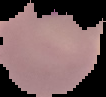
Summary:
  - Preparation: thin blood film
  - Image size: 106×97 pixels
  - Image type: cell region segmented out of the field of view; surrounding area masked to black
  - Result: Plasmodium parasites identified